State the blood parasite species.
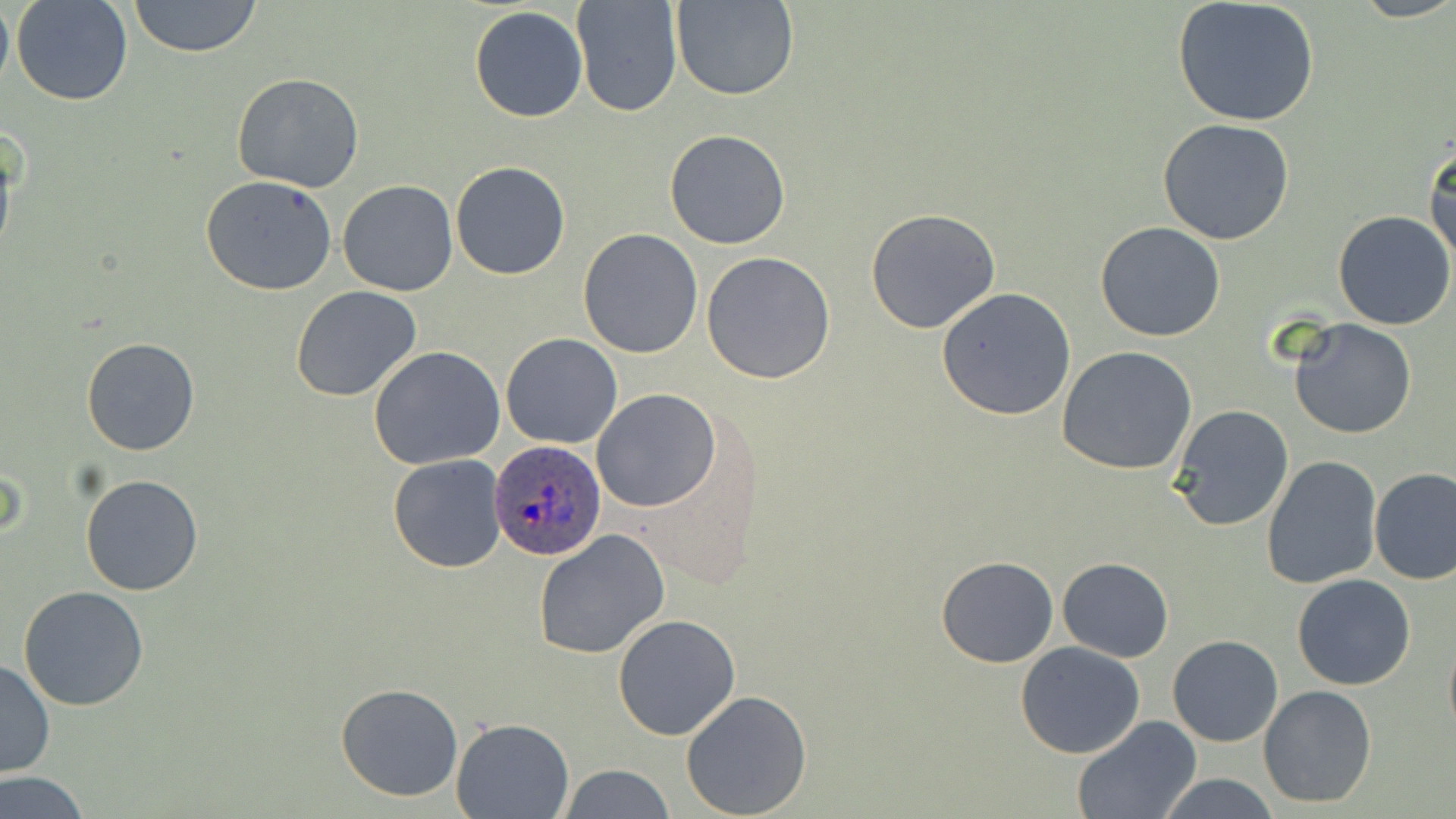

Plasmodium ovale.

Approximate bounding boxes as (x1, y1, x2, y2) in pixels. Plasmodium ovale-infected red blood cell locations: (489, 440, 607, 562). Uninfected red blood cell locations: (0, 0, 13, 99), (11, 0, 133, 106), (128, 0, 260, 58), (571, 0, 681, 117), (673, 0, 799, 101), (1172, 1, 1321, 126), (470, 6, 588, 123), (232, 72, 365, 191), (1158, 118, 1295, 245), (664, 128, 791, 249), (1424, 140, 1456, 266), (450, 161, 571, 281), (201, 176, 337, 295), (338, 180, 457, 297), (866, 208, 1002, 334), (1333, 209, 1455, 331), (1095, 222, 1226, 342), (578, 228, 705, 359), (701, 251, 836, 384), (291, 285, 422, 402), (935, 287, 1076, 422), (1288, 318, 1419, 440), (501, 333, 623, 450), (81, 337, 200, 456), (1057, 345, 1197, 474), (368, 346, 506, 468), (592, 388, 722, 512), (1169, 406, 1295, 531), (388, 454, 506, 572), (1261, 456, 1382, 590), (1369, 467, 1456, 585), (79, 473, 204, 595), (534, 529, 669, 659), (936, 555, 1059, 668), (1057, 557, 1172, 662), (1293, 575, 1417, 691), (18, 586, 150, 712), (613, 613, 742, 742), (1442, 628, 1456, 743), (1167, 635, 1284, 747), (1014, 641, 1146, 759), (0, 660, 55, 777), (335, 681, 465, 802), (1258, 684, 1378, 809), (681, 690, 812, 818), (1071, 715, 1202, 819), (451, 718, 574, 818), (559, 765, 675, 819), (2, 772, 88, 818), (1151, 772, 1287, 818). Optical microscopy. Thin blood smear. Captured at 1000x magnification. Image is 1456×819 pixels. Single field of view. May-Grünwald-Giemsa stain.